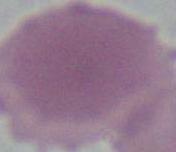

Captured at 1000x magnification. An erythrocyte is seen. Photomicrograph.